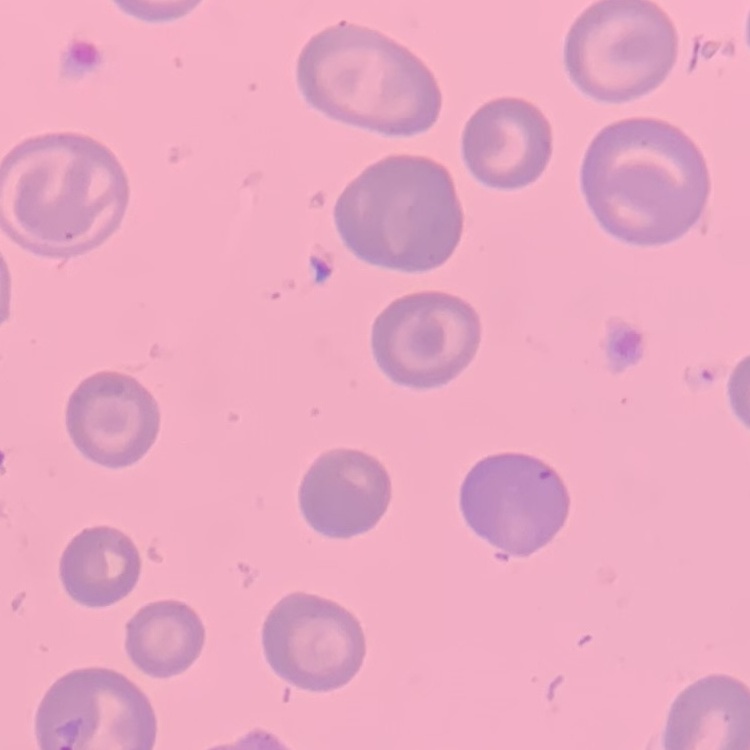
{
  "erythrocyte_morphology": "no rouleaux formation",
  "preparation": "thin blood smear",
  "stain": "Field's or Giemsa",
  "image_type": "one tile cut from a larger photomicrograph"
}